Identify the cell.
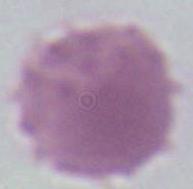

This is an erythrocyte.

Summary:
  - Magnification: 1000x
  - Modality: micrograph